Assess this cell for malaria.
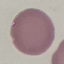

Uninfected.

Cell patch, automatically extracted from a larger field of view and resized to 64 × 64 pixels. Acquired by smartphone through the microscope eyepiece. Thin smear of blood. Giemsa stain.